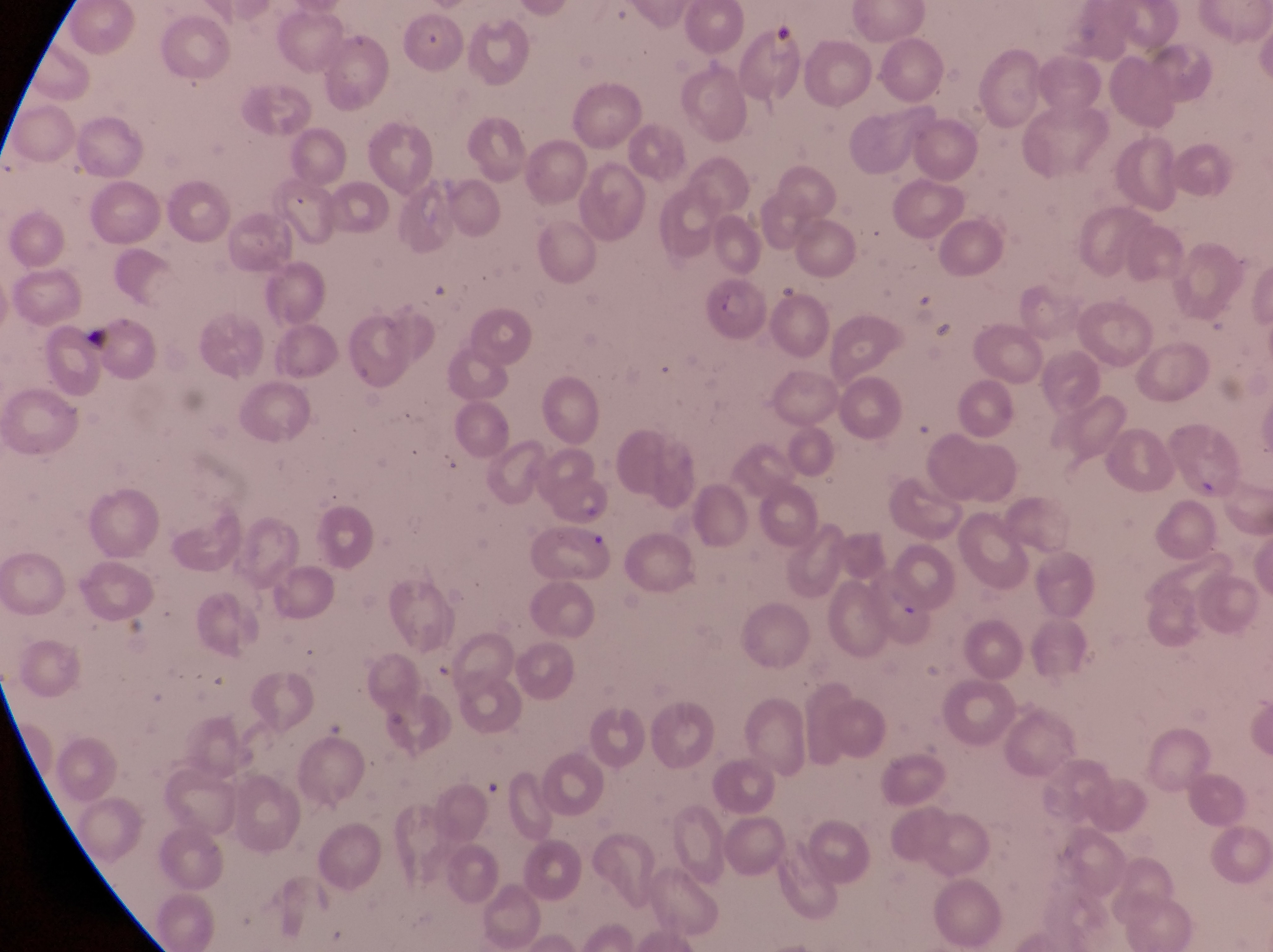

Approximate bounding boxes as {left, top, right, bottom} in pixels.
Summary:
  - Parasitised red blood cell locations: {708, 274, 773, 344}, {546, 469, 611, 532}
  - Artifact (platelet-like body, stain precipitate, or debris) locations: {759, 18, 796, 61}, {77, 315, 117, 352}
  - Country: Uganda
  - Field of view: single
  - Magnification: 1000x
  - Image size: 1273×952 pixels
  - Preparation: thin blood film
  - Capture: smartphone photograph through the eyepiece of an Olympus CX-23 microscope